Report the malaria status of this cell.
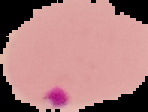

It is parasitized.

Image is 148×112 pixels. From a thin blood smear. Segmented cell region on a black background.